State the blood parasite species.
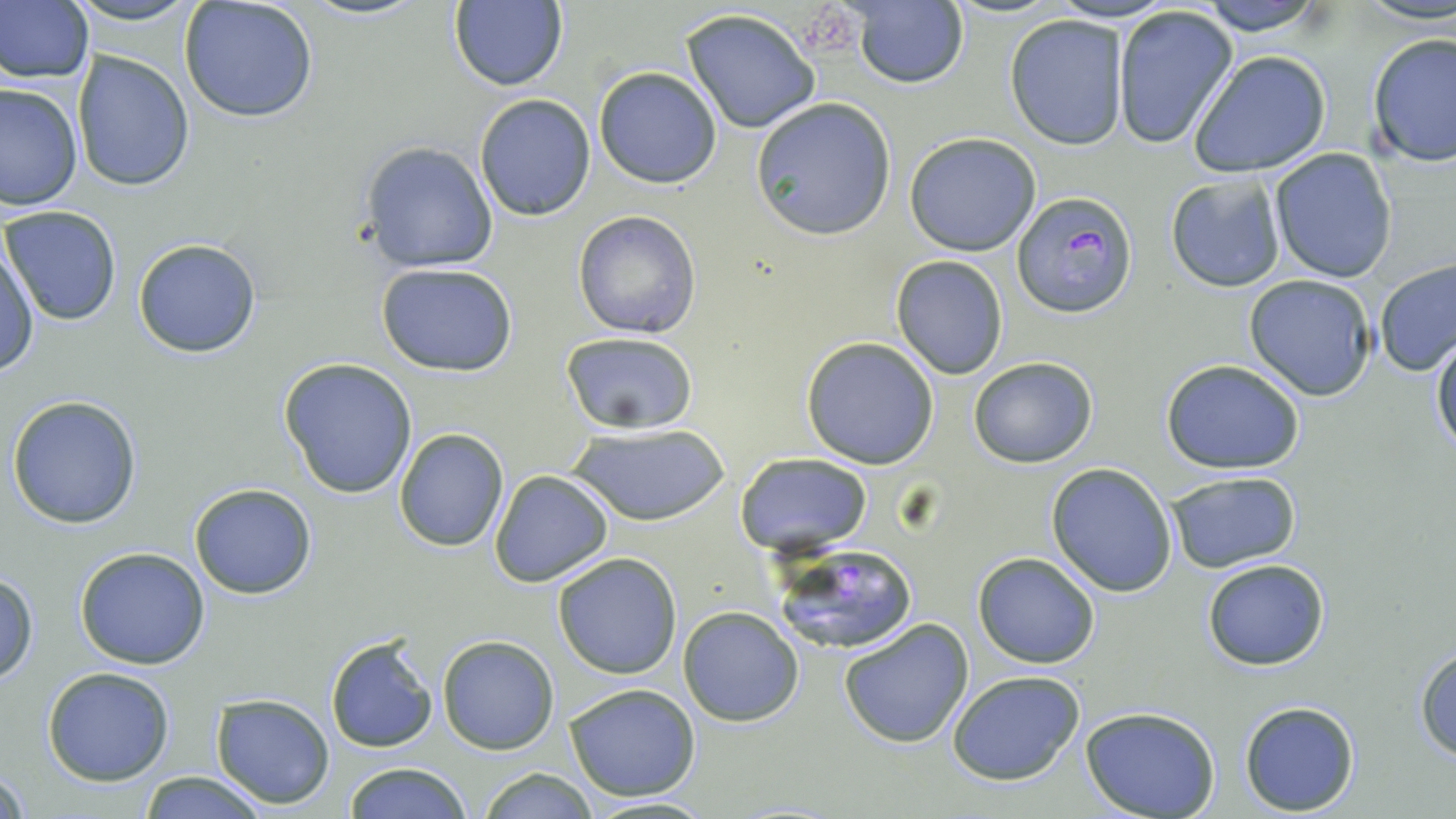

Plasmodium falciparum.

image size = 1456×819 pixels
uninfected red blood cell locations = approximate bounding boxes as (x1,y1)-(x2,y2) corner pairs in pixels: (177,0)-(319,123), (1192,0)-(1331,36), (845,1)-(971,91), (448,2)-(569,92), (0,3)-(94,85), (1110,4)-(1239,150), (680,8)-(823,134), (1004,14)-(1129,151), (1366,33)-(1456,168), (72,50)-(194,192), (1189,51)-(1332,178), (592,66)-(723,189), (0,80)-(82,210), (474,93)-(596,221), (750,98)-(897,241), (903,132)-(1043,257), (358,140)-(497,274), (1269,148)-(1400,284), (1165,173)-(1286,291), (3,205)-(123,326), (573,209)-(702,339), (1,233)-(38,378), (133,239)-(261,357), (890,256)-(1010,380), (1376,259)-(1456,375), (374,262)-(520,378), (1243,273)-(1376,402), (1430,332)-(1455,458), (560,334)-(699,436), (801,336)-(941,469), (967,356)-(1098,468), (278,357)-(418,499), (1161,358)-(1306,474), (7,394)-(144,529), (565,422)-(731,529), (393,427)-(509,551), (736,452)-(872,557), (1047,462)-(1178,596), (488,469)-(615,588), (1164,469)-(1302,574), (189,482)-(317,599), (74,547)-(211,670), (552,552)-(682,678), (973,552)-(1100,669), (1202,558)-(1330,671), (0,570)-(39,684), (678,606)-(804,726), (838,619)-(973,750), (325,635)-(438,754), (436,636)-(559,754), (1414,644)-(1456,763), (43,666)-(176,786), (946,671)-(1085,786), (564,682)-(701,802), (210,692)-(337,809), (1239,700)-(1361,815), (1081,708)-(1221,819), (343,762)-(473,818), (2,763)-(30,818), (476,767)-(598,819), (138,771)-(269,818), (576,796)-(721,817)
field of view = one of a larger specimen
modality = optical microscopy
preparation = thin blood smear
magnification = 1000x
platelet locations = approximate bounding boxes as (x1,y1)-(x2,y2) corner pairs in pixels: (798,5)-(859,68)
Plasmodium falciparum-infected red blood cell locations = approximate bounding boxes as (x1,y1)-(x2,y2) corner pairs in pixels: (1013,190)-(1137,319), (764,539)-(921,658)
stain = May-Grünwald-Giemsa